Outline each blood parasite and name the species.
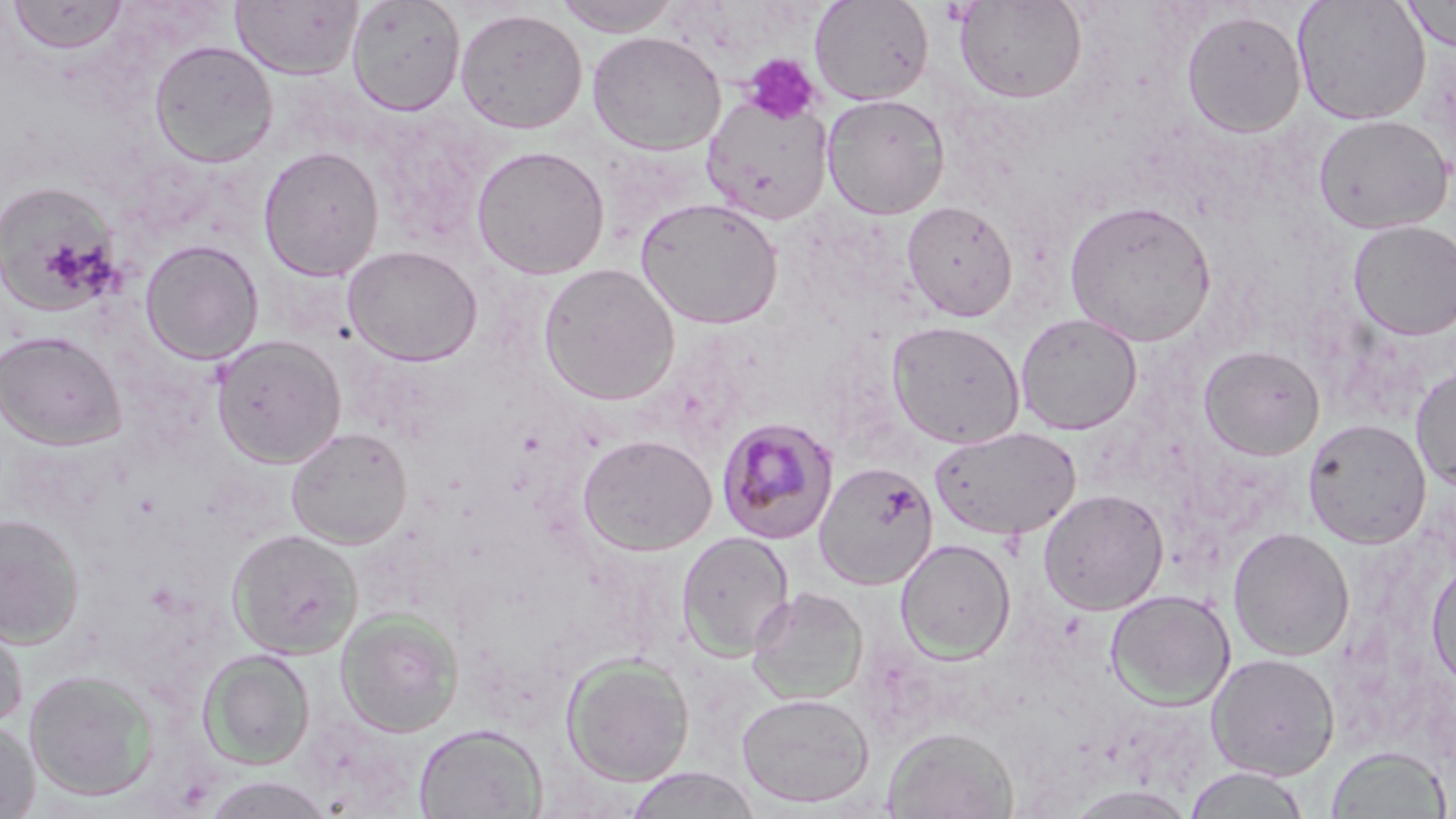
Approximate bounding boxes as [x1, y1, x2, y2] in pixels.
Plasmodium malariae-infected red blood cells: [716, 417, 840, 545].
No Plasmodium falciparum, Plasmodium ovale, Plasmodium vivax, Babesia divergens, or Trypanosoma brucei observed.

Summary:
  - Platelet locations: [741, 54, 822, 125]
  - Uninfected red blood cell locations: [6, 0, 128, 53], [346, 0, 465, 116], [552, 0, 682, 36], [809, 0, 933, 105], [953, 0, 1087, 103], [1292, 0, 1431, 125], [1400, 0, 1456, 52], [231, 1, 364, 80], [454, 8, 587, 135], [1181, 8, 1307, 140], [586, 31, 726, 156], [149, 40, 278, 168], [821, 93, 951, 220], [702, 94, 832, 225], [1313, 114, 1454, 234], [471, 145, 610, 280], [258, 146, 384, 281], [0, 181, 122, 317], [635, 196, 784, 329], [901, 200, 1019, 322], [1064, 200, 1217, 347], [1348, 220, 1456, 340], [140, 239, 263, 364], [343, 245, 482, 366], [537, 263, 680, 405], [1015, 313, 1143, 435], [886, 320, 1026, 449], [0, 330, 125, 450], [211, 334, 346, 468], [1198, 345, 1325, 460], [1410, 367, 1456, 491], [1303, 417, 1431, 548], [929, 425, 1081, 541], [286, 427, 412, 549], [578, 433, 717, 556], [813, 460, 938, 590], [1038, 488, 1169, 615], [0, 513, 84, 647], [1227, 526, 1355, 661], [227, 528, 363, 660], [676, 530, 795, 661], [895, 539, 1016, 662], [1426, 558, 1456, 691], [747, 586, 868, 705], [1105, 589, 1236, 709], [0, 607, 29, 730], [336, 609, 463, 737], [198, 649, 316, 770], [1206, 653, 1341, 780], [561, 655, 695, 786], [24, 669, 159, 802], [735, 692, 875, 809], [0, 716, 39, 818], [414, 723, 547, 819], [884, 726, 1018, 819], [1326, 745, 1449, 818], [1183, 766, 1312, 818], [623, 767, 762, 819], [200, 775, 334, 818], [1064, 785, 1199, 818]
  - Slide-level diagnosis: Plasmodium malariae
  - Field of view: one of a larger specimen
  - Preparation: thin blood smear
  - Magnification: 1000x
  - Modality: optical microscopy
  - Image size: 1456×819 pixels
  - Stain: May-Grünwald-Giemsa